Rate the background quality.
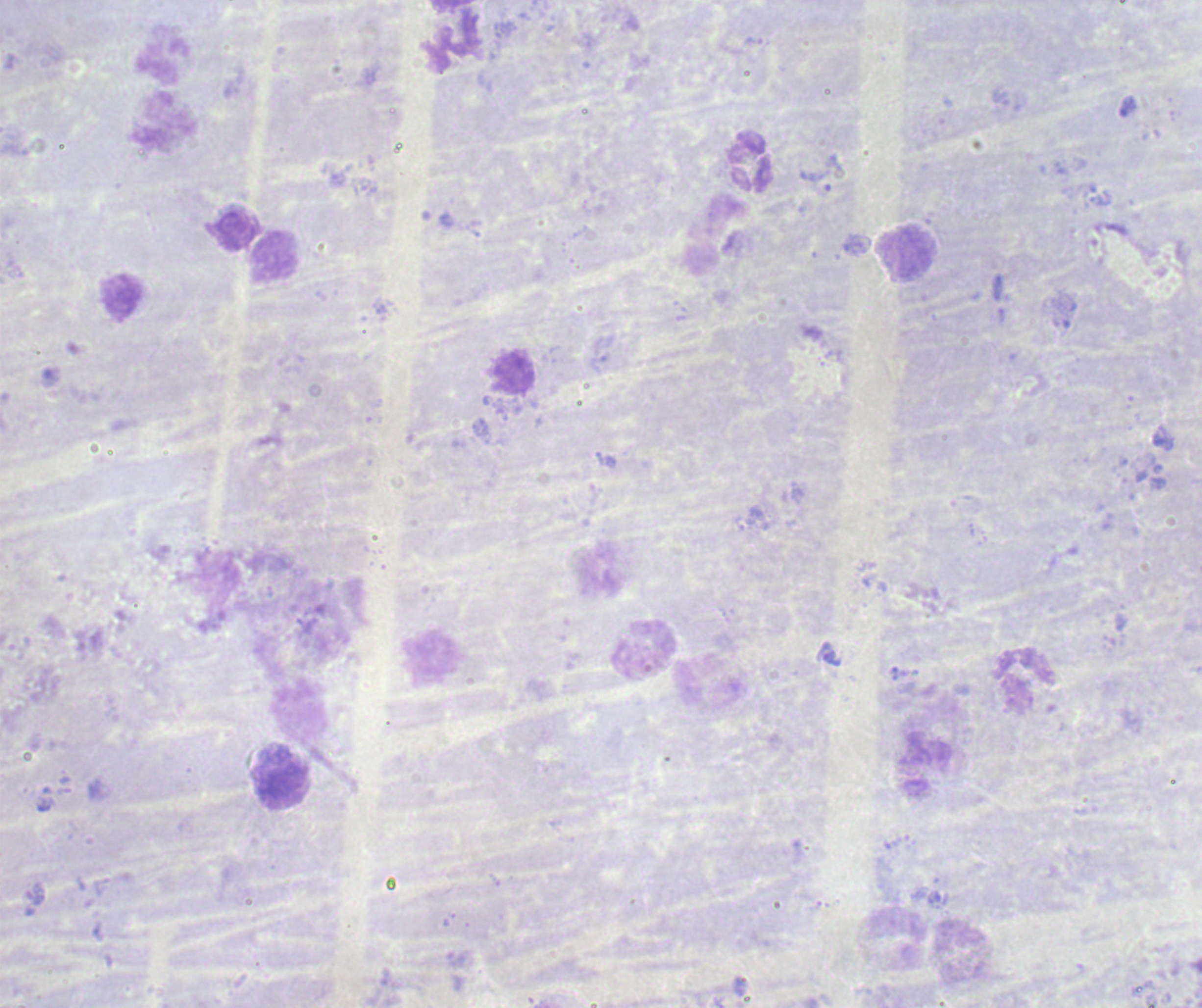
Poor.

Approximate centers as [x, y] in pixels.
Summary:
  - Leukocyte locations: [749, 163], [907, 254], [274, 258], [643, 648], [1026, 679]
  - Magnification: 100x
  - Result: no malaria parasites seen
  - Preparation: thick blood smear
  - Context: previously used in a real diagnosis
  - Stain: Romanowsky
  - Image size: 1202×1008 pixels
  - Field of view: one from this slide